Locate every Plasmodium ovale-infected red blood cell.
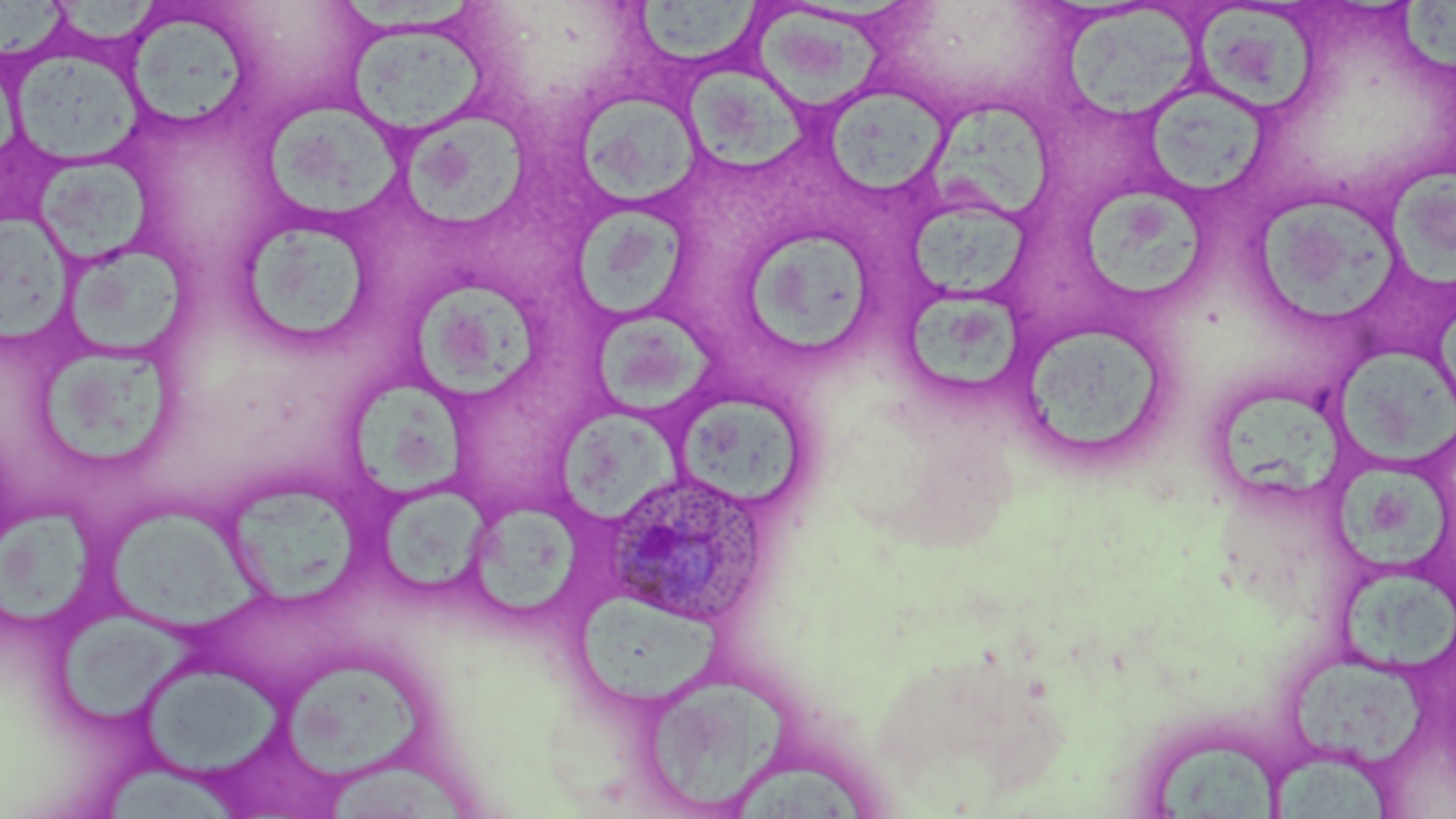

Approximate bounding boxes as (x1,y1)-(x2,y2) corner pairs in pixels.
Plasmodium ovale-infected red blood cells: (603,468)-(766,628).

slide-level diagnosis = Plasmodium ovale
uninfected red blood cell locations = approximate bounding boxes as (x1,y1)-(x2,y2) corner pairs in pixels: (1,0)-(67,58), (56,0)-(166,48), (634,0)-(768,62), (1197,3)-(1321,115), (1394,3)-(1456,78), (1068,5)-(1207,117), (753,10)-(890,115), (123,15)-(251,128), (342,18)-(493,140), (10,48)-(146,167), (682,69)-(810,176), (827,86)-(956,198), (1156,90)-(1271,196), (574,91)-(700,208), (932,101)-(1051,220), (268,103)-(403,215), (408,113)-(531,227), (37,155)-(155,263), (1392,168)-(1456,294), (1082,188)-(1203,301), (1259,192)-(1398,321), (912,204)-(1032,301), (566,207)-(692,320), (3,210)-(79,347), (232,214)-(381,352), (745,232)-(874,357), (59,238)-(194,360), (410,283)-(546,403), (901,290)-(1030,400), (591,316)-(725,418), (1013,321)-(1172,466), (42,348)-(172,467), (1337,349)-(1456,460), (355,388)-(472,503), (1219,389)-(1342,502), (678,395)-(802,507), (558,407)-(685,521), (1334,464)-(1455,572), (232,486)-(354,616), (386,486)-(495,596), (0,501)-(94,636), (472,505)-(580,617), (106,509)-(267,632), (1338,573)-(1456,671), (575,597)-(728,710), (55,615)-(212,729), (1290,654)-(1425,767), (280,660)-(430,785), (137,663)-(288,773), (639,673)-(789,815), (1154,741)-(1278,818), (1272,753)-(1397,819), (323,758)-(479,819), (736,761)-(865,819), (107,763)-(237,819)
field of view = one of a larger specimen
magnification = 1000x
preparation = thin blood film
image size = 1456×819 pixels
stain = May-Grünwald-Giemsa
modality = light microscopy